Report the malaria status of this cell.
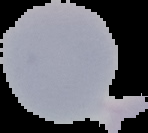

It is uninfected.

Summary:
  - Image type: segmented cell region with the area outside set to black
  - Image size: 148×133 pixels
  - Preparation: thin blood film